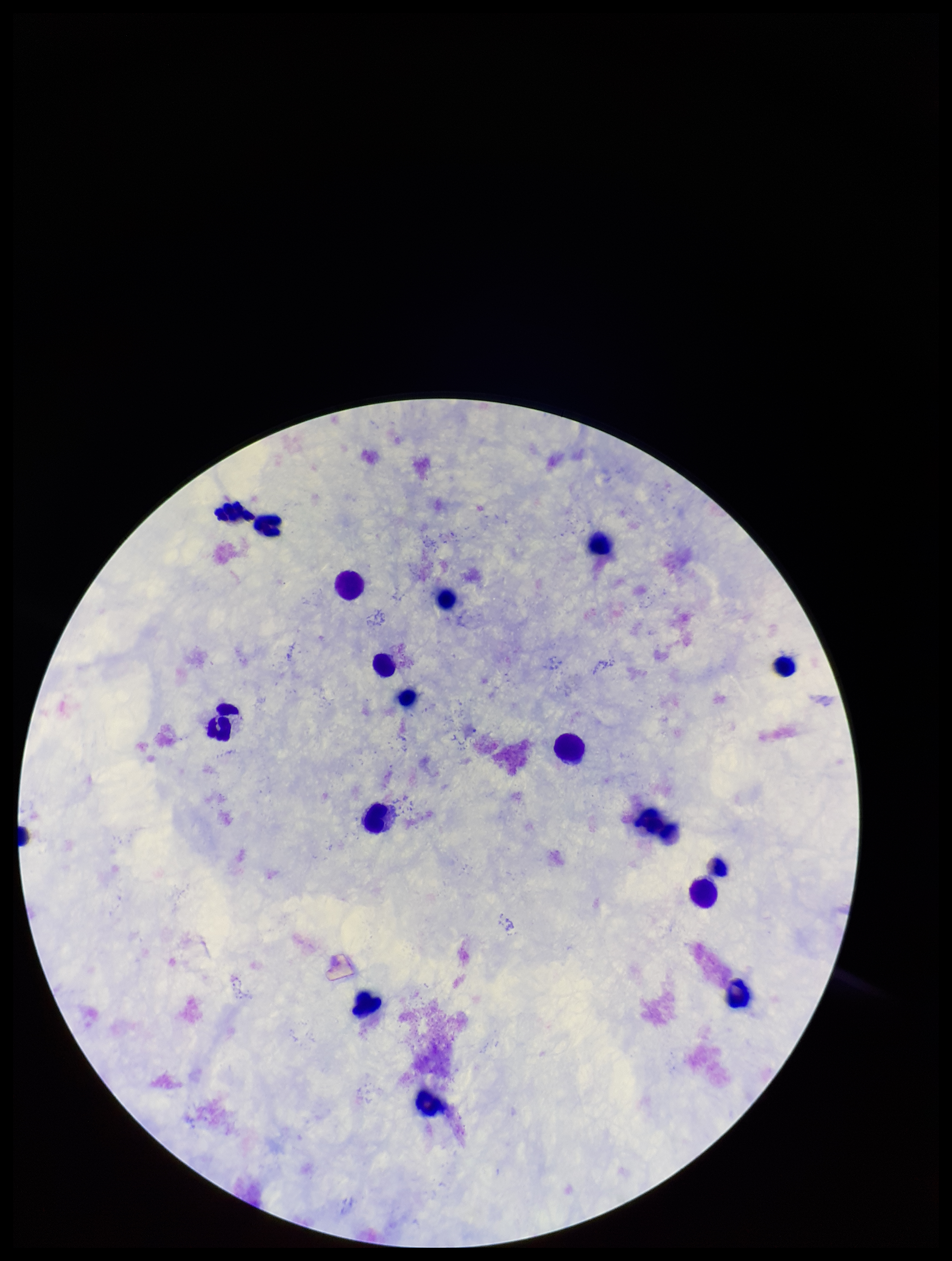

Summary:
  - Preparation: thick blood smear
  - Capture: smartphone photograph through the microscope eyepiece
  - Image size: 952×1261 pixels
  - Field of view: single
  - Leukocyte count: 15
  - Parasite count: 0
  - Stain: Giemsa
  - Patient malaria status: negative
  - Plasmodium parasites: none identified